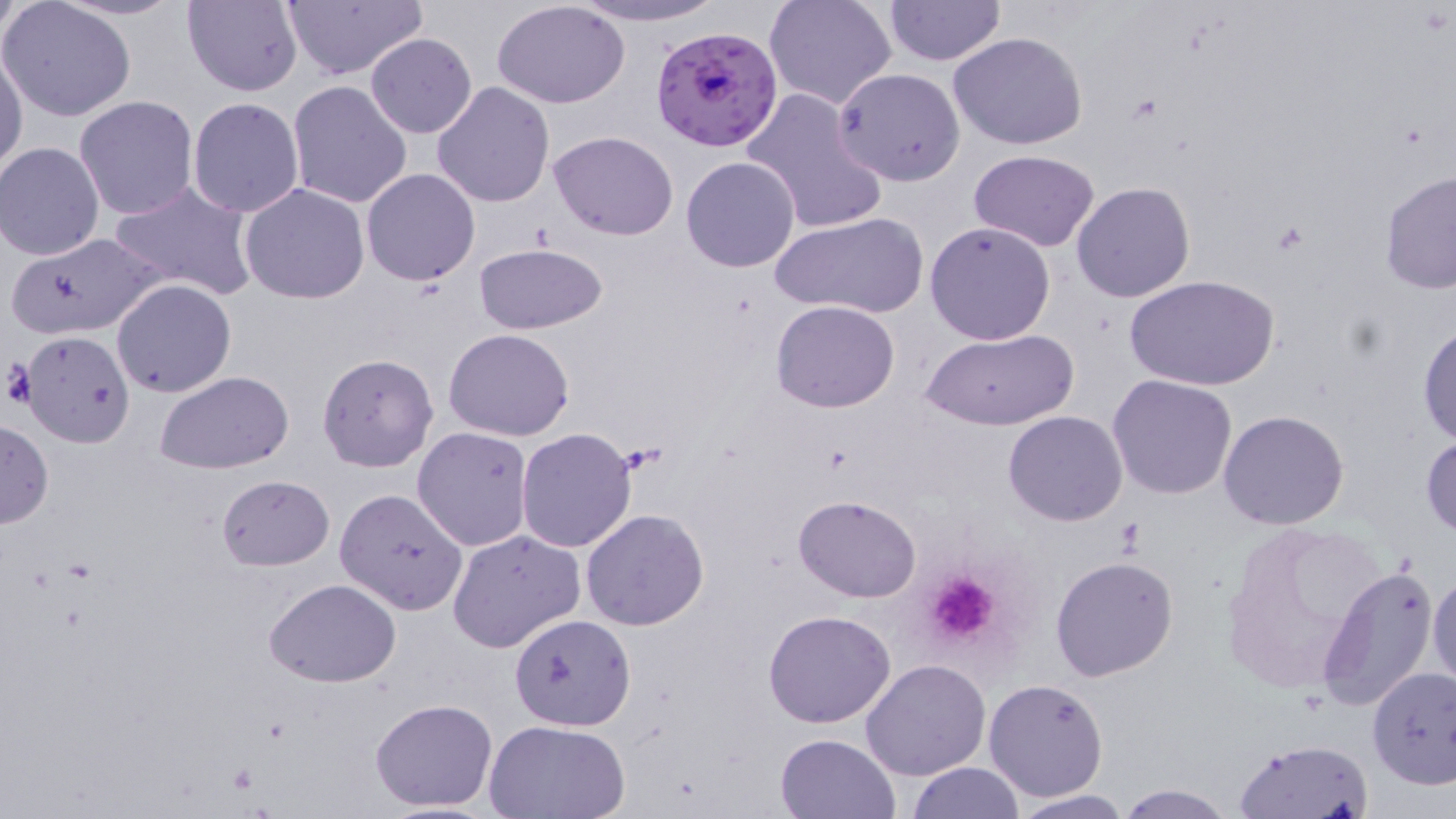 Approximate bounding boxes as (x1, y1, x2, y2) in pixels. Plasmodium falciparum-infected red blood cell locations: (652, 26, 783, 152). Platelet locations: (921, 570, 1001, 645), (223, 761, 260, 798). Uninfected red blood cell locations: (182, 0, 304, 96), (281, 0, 429, 82), (763, 0, 898, 111), (884, 0, 1004, 65), (1, 1, 137, 122), (565, 1, 727, 28), (494, 2, 630, 108), (366, 33, 477, 137), (949, 33, 1090, 150), (0, 46, 27, 180), (834, 67, 966, 185), (287, 80, 414, 209), (432, 81, 556, 207), (741, 88, 889, 235), (74, 96, 198, 219), (188, 97, 305, 218), (548, 131, 677, 240), (1, 142, 106, 260), (970, 150, 1099, 251), (681, 156, 801, 272), (360, 168, 480, 287), (1378, 170, 1456, 295), (109, 180, 257, 302), (1071, 181, 1196, 302), (240, 184, 370, 303), (769, 212, 928, 319), (925, 222, 1056, 345), (6, 233, 161, 339), (472, 243, 609, 335), (1124, 273, 1281, 390), (112, 279, 237, 398), (770, 300, 900, 414), (1416, 319, 1456, 446), (444, 329, 576, 441), (923, 329, 1078, 432), (19, 330, 135, 447), (317, 354, 438, 472), (156, 372, 297, 472), (1108, 375, 1238, 499), (1218, 410, 1350, 530), (1004, 412, 1128, 525), (0, 417, 52, 528), (412, 428, 532, 551), (515, 428, 638, 553), (1420, 433, 1455, 541), (217, 474, 334, 569), (336, 489, 467, 614), (794, 495, 921, 601), (580, 509, 709, 629), (1215, 520, 1388, 696), (447, 530, 586, 653), (1051, 555, 1179, 682), (1315, 563, 1439, 712), (1429, 567, 1456, 693), (264, 577, 403, 687), (763, 610, 896, 728), (509, 613, 637, 731), (861, 659, 991, 781), (1368, 666, 1456, 788), (983, 679, 1110, 802), (369, 697, 498, 812), (484, 719, 632, 817), (774, 732, 902, 819), (1233, 736, 1376, 817), (906, 761, 1024, 818), (1114, 781, 1235, 818), (1007, 790, 1134, 819). Slide-level diagnosis: Plasmodium falciparum. Optical microscopy. 1000x magnification. Thin blood film. Image is 1456×819 pixels. May-Grünwald-Giemsa stain. One field of a larger specimen.